Name the cell type shown.
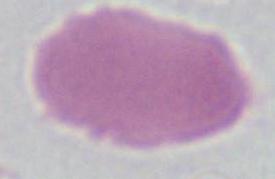

This is an erythrocyte.

Photomicrograph. 1000x magnification.